State the blood parasite species.
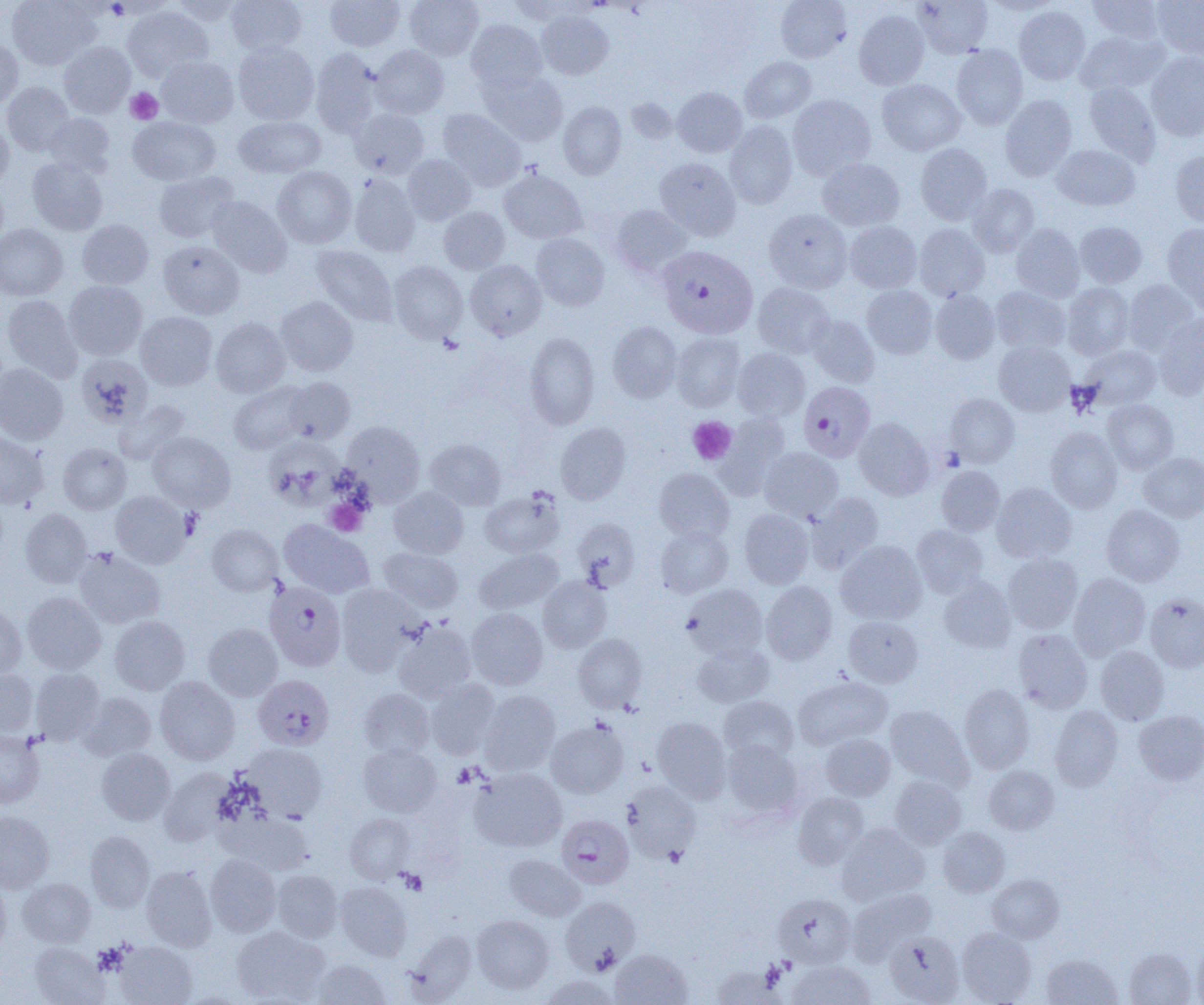
Plasmodium falciparum.

Approximate bounding boxes as (x1,y1)-(x2,y2) corner pairs in pixels. Platelet locations: (125,87)-(163,124), (687,416)-(737,465), (325,500)-(368,536), (398,869)-(427,894). Uninfected red blood cell locations: (7,0)-(101,70), (169,0)-(244,25), (225,0)-(307,56), (325,0)-(404,51), (404,0)-(483,60), (505,0)-(585,23), (776,0)-(851,62), (913,0)-(993,58), (1086,0)-(1166,43), (1152,0)-(1204,60), (122,6)-(213,82), (1014,6)-(1091,85), (536,10)-(614,80), (854,10)-(929,89), (466,20)-(547,92), (1074,29)-(1168,95), (0,39)-(23,110), (59,41)-(136,118), (233,41)-(319,125), (371,45)-(449,118), (952,45)-(1028,129), (310,48)-(381,137), (1146,52)-(1204,140), (156,56)-(239,127), (740,57)-(816,123), (479,69)-(568,146), (877,79)-(965,156), (2,81)-(74,156), (1084,82)-(1161,164), (673,87)-(746,157), (788,94)-(876,179), (1000,95)-(1077,181), (558,101)-(626,179), (351,109)-(429,178), (438,109)-(525,190), (44,113)-(115,177), (0,116)-(14,189), (128,116)-(220,185), (234,116)-(325,178), (724,120)-(797,208), (915,143)-(992,223), (1052,144)-(1140,211), (1170,151)-(1204,228), (402,154)-(476,225), (27,156)-(109,235), (654,157)-(741,240), (817,158)-(905,231), (273,166)-(356,248), (499,168)-(587,244), (153,171)-(239,243), (349,174)-(420,256), (0,177)-(9,251), (968,183)-(1040,257), (207,196)-(292,277), (611,205)-(693,276), (439,206)-(510,274), (763,208)-(852,292), (77,219)-(154,289), (1075,221)-(1147,288), (845,222)-(922,293), (1162,223)-(1204,307), (0,224)-(68,300), (914,224)-(990,301), (1011,224)-(1085,302), (531,233)-(609,310), (158,240)-(244,319), (311,245)-(397,326), (465,260)-(546,340), (389,261)-(467,343), (1122,279)-(1200,354), (64,281)-(147,360), (752,283)-(834,358), (1063,283)-(1134,359), (862,285)-(937,359), (991,286)-(1070,354), (930,289)-(1000,364), (2,294)-(82,382), (276,296)-(357,376), (135,311)-(217,391), (806,314)-(879,388), (1154,314)-(1204,399), (211,317)-(290,397), (607,321)-(682,403), (525,332)-(600,429), (671,333)-(745,411), (993,341)-(1075,416), (1081,345)-(1161,410), (732,348)-(810,421), (76,353)-(153,427), (0,363)-(68,445), (284,377)-(355,444), (229,382)-(310,455), (945,393)-(1019,468), (114,399)-(190,464), (1102,399)-(1178,475), (713,411)-(791,499), (854,418)-(934,499), (341,422)-(425,505), (556,423)-(631,504), (1045,426)-(1122,513), (147,432)-(235,512), (0,433)-(50,509), (265,435)-(345,505), (425,439)-(506,510), (58,443)-(131,515), (760,447)-(843,521), (1138,452)-(1204,522), (936,466)-(1005,535), (654,468)-(733,543), (992,482)-(1077,563), (389,487)-(468,559), (110,490)-(192,569), (480,490)-(563,558), (807,492)-(884,571), (1102,504)-(1184,587), (20,508)-(92,587), (739,509)-(814,588), (573,518)-(640,591), (279,520)-(374,598), (206,525)-(284,596), (911,525)-(988,598), (656,526)-(732,598), (836,540)-(927,625), (73,547)-(165,629), (379,548)-(463,612), (474,548)-(562,613), (1003,553)-(1082,633), (1069,573)-(1150,659), (538,576)-(612,653), (938,576)-(1016,653), (761,580)-(838,664), (683,584)-(767,660), (336,585)-(420,675), (22,592)-(106,674), (1145,593)-(1204,672), (0,601)-(27,680), (466,607)-(547,690), (109,616)-(190,694), (843,616)-(923,687), (393,622)-(476,703), (203,623)-(283,701), (1013,629)-(1092,713), (574,633)-(647,712), (691,641)-(773,707), (1095,646)-(1169,724), (0,668)-(39,737), (31,668)-(105,744), (154,676)-(240,765), (793,676)-(892,750), (425,679)-(501,759), (959,684)-(1035,773), (359,688)-(434,759), (478,690)-(561,775), (77,692)-(156,760), (719,696)-(799,763), (885,705)-(973,790), (1050,706)-(1123,791), (1134,710)-(1204,785), (652,717)-(730,802), (546,720)-(628,798), (0,730)-(45,809), (821,733)-(895,801), (721,740)-(803,819), (241,743)-(327,822), (358,744)-(442,817), (96,748)-(175,825), (984,766)-(1058,834), (159,767)-(236,845), (470,767)-(567,852), (890,776)-(966,849), (621,780)-(701,864), (792,792)-(869,868), (0,811)-(54,893), (227,811)-(315,875), (345,813)-(415,883), (837,823)-(930,905), (938,827)-(1010,897), (85,831)-(155,911), (205,854)-(281,937), (504,854)-(585,921), (141,865)-(217,951), (272,870)-(342,941), (988,874)-(1063,943), (0,877)-(11,958), (17,878)-(96,947), (335,881)-(412,960), (847,887)-(936,965), (774,893)-(855,968), (560,896)-(640,974), (473,915)-(554,994), (231,925)-(328,1004), (957,927)-(1036,1004), (405,929)-(477,1002), (884,931)-(965,1004), (29,942)-(108,1004), (114,942)-(197,1005), (1193,942)-(1204,1005), (1124,947)-(1197,1005), (610,948)-(692,1005), (1040,953)-(1123,1005), (311,959)-(391,1004), (787,960)-(875,1005), (709,964)-(784,1004), (541,974)-(620,1005). Plasmodium falciparum-infected red blood cell locations: (657,245)-(758,338), (799,381)-(875,462), (265,582)-(346,671), (253,675)-(334,750), (556,814)-(634,889). Optical microscopy. One field of a larger specimen. Captured at 1000x magnification. Thin blood film. Image is 1204×1005 pixels.